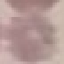

{
  "result": "no malaria parasites seen",
  "preparation": "thin blood smear",
  "image_type": "cell patch, automatically extracted from a larger field of view and resized to 64 × 64 pixels",
  "capture": "smartphone camera at the microscope eyepiece",
  "stain": "Giemsa"
}